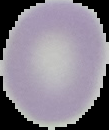

result = no malaria parasites seen
image type = segmented cell region on a black background
image size = 109×130 pixels
preparation = thin blood film